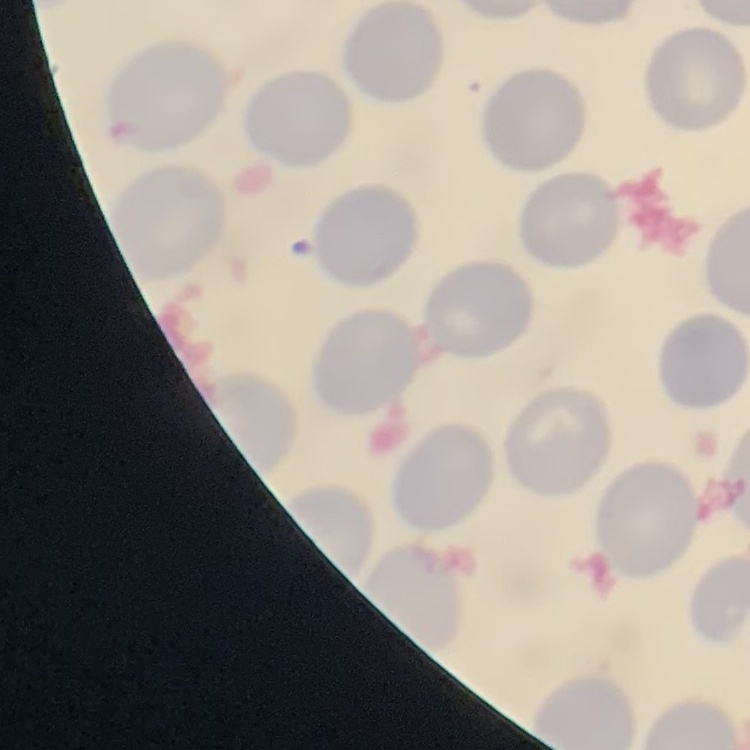

Summary:
  - Erythrocyte morphology: no rouleaux formation
  - Image type: square crop of a larger photomicrograph
  - Preparation: thin peripheral smear
  - Stain: Field's or Giemsa